Classify this cell by malaria status.
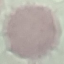

It is uninfected.

image_type: automatically extracted cell patch, resized to 64 × 64 pixels
preparation: thin smear
stain: Giemsa
capture: smartphone camera at the microscope eyepiece